Describe the morphology of the erythrocytes.
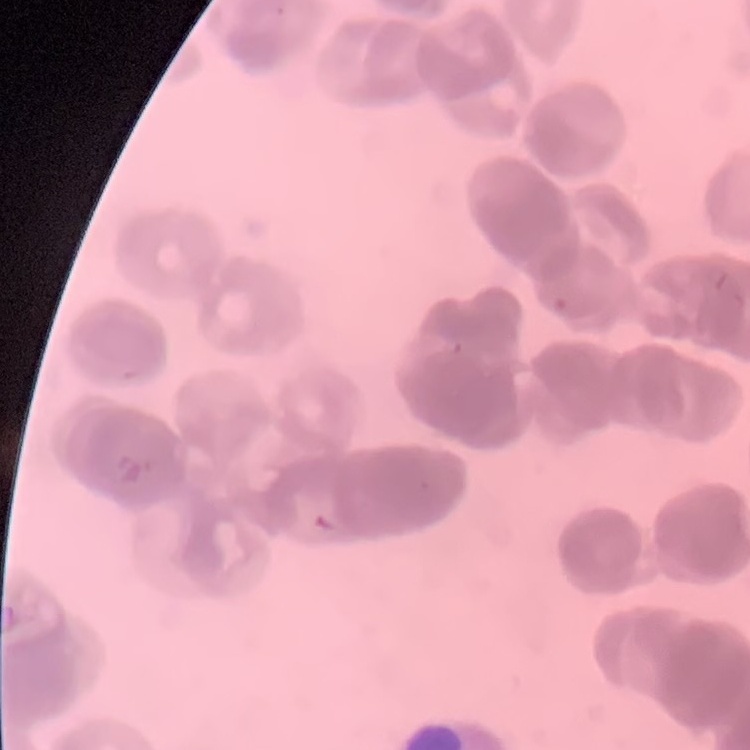

Rouleaux formation.

preparation: thin peripheral smear
image_type: one tile cut from a larger photomicrograph
stain: Field's or Giemsa